Report the malaria status of this cell.
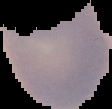

It is uninfected.

From a thin blood film. Image is 112×109 pixels. Segmented cell region on a black background.